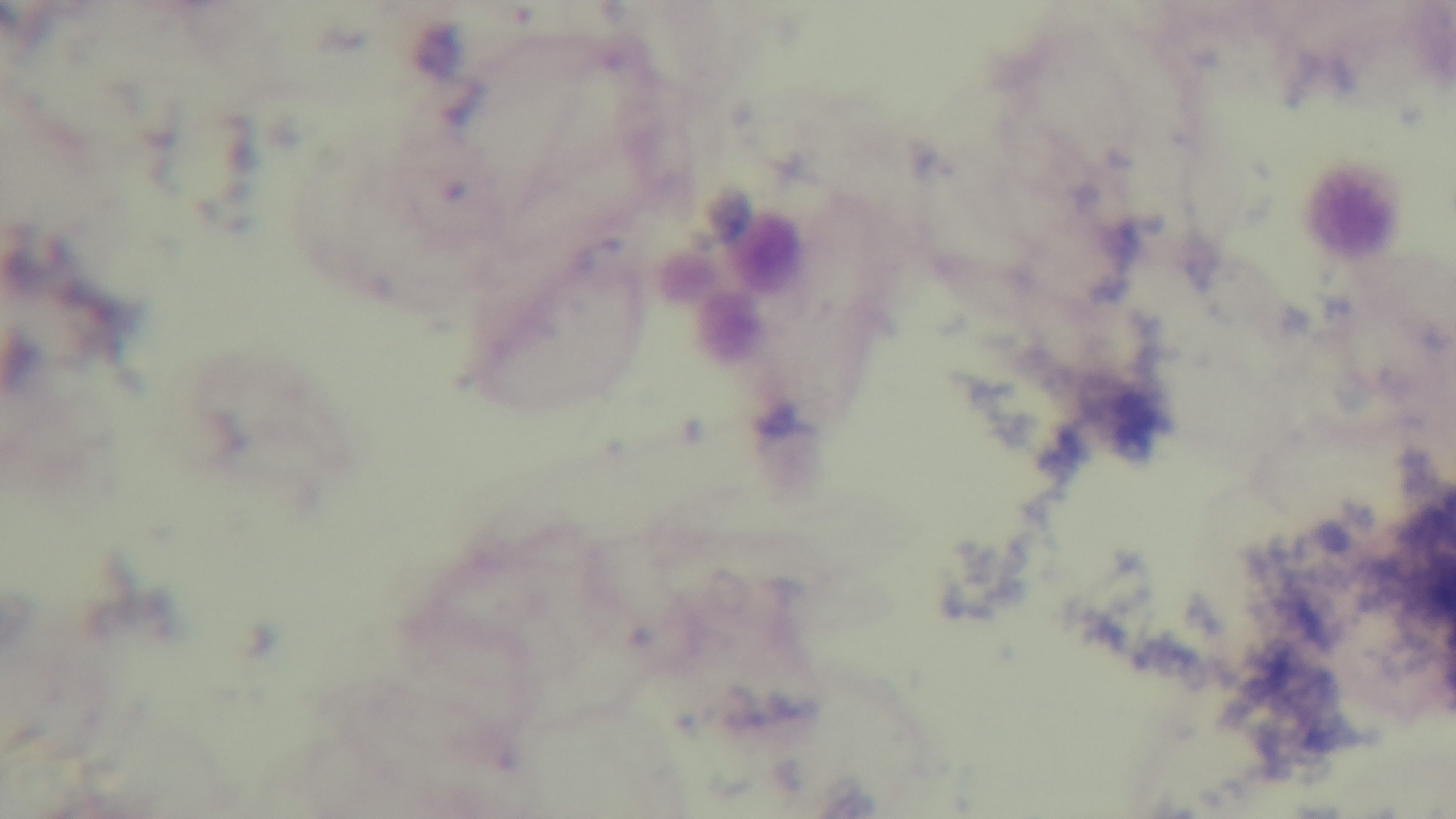

Oil-immersion objective, 100x. Preparation: thick smear. Photomicrograph. Single field of view. Malaria status: uninfected. Mounted 4K digital camera. Giemsa-stained.